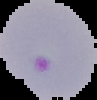
Malaria status: parasitized. From a thin blood smear. Segmented cell region on a black background. Image is 97×100 pixels.